Describe the morphology of the red blood cells.
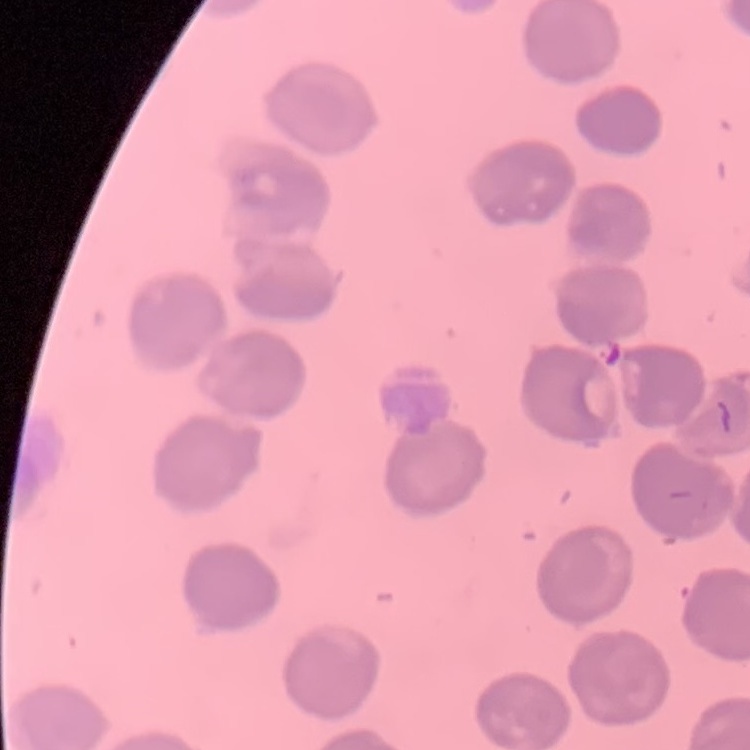
No rouleaux formation.

{
  "stain": "Field's or Giemsa",
  "preparation": "thin peripheral smear",
  "image_type": "one tile cut from a larger photomicrograph"
}